State which parasite is depicted.
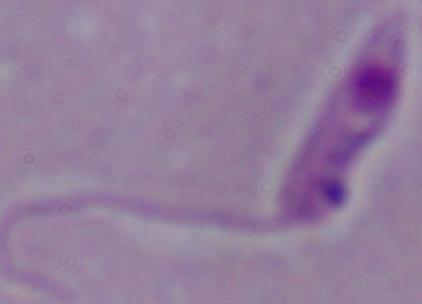
This is Leishmania.

modality: micrograph
magnification: 1000x